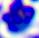

{
  "modality": "photomicrograph",
  "identification": "leukocyte",
  "magnification": "400x"
}